State which cell type is depicted.
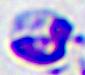
A leukocyte.

modality = photomicrograph
magnification = 400x